Assess for Plasmodium parasites.
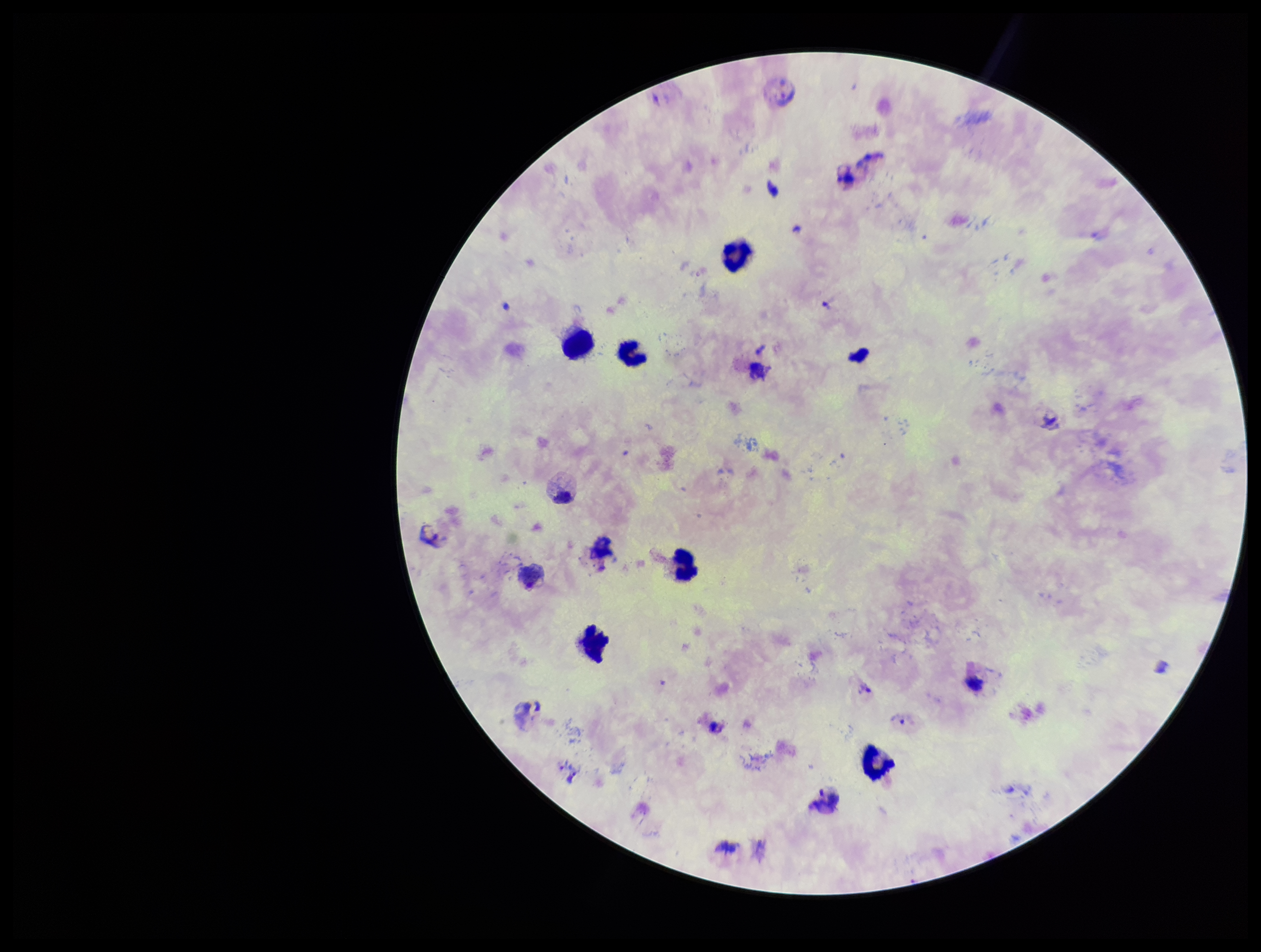

Detected.

Summary:
  - Preparation: thick blood smear
  - Capture: smartphone photograph through the microscope eyepiece
  - Leukocyte count: 9
  - Patient malaria status: positive
  - Field of view: one from this slide
  - Image size: 1261×952 pixels
  - Species reported for this patient: Plasmodium vivax
  - Parasite count: 2
  - Stain: Giemsa